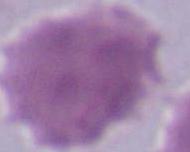
Photomicrograph. An erythrocyte is seen. 1000x magnification.